Outline each blood parasite and name the species.
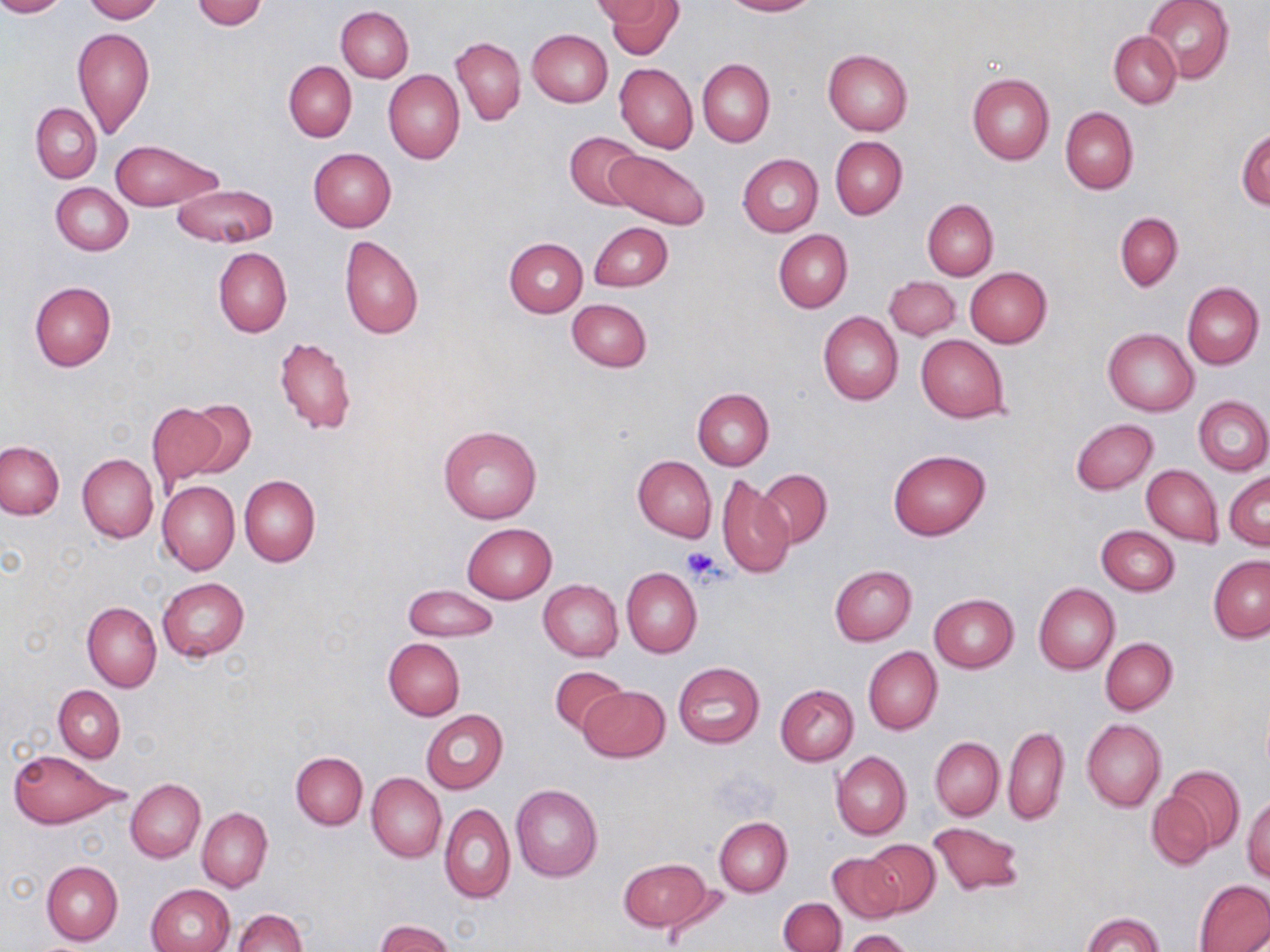
No blood parasites observed.

Summary:
  - Coordinate format: approximate bounding boxes as [x1, y1, x2, y2] in pixels
  - Uninfected red blood cell locations: [0, 0, 66, 17], [83, 0, 161, 22], [192, 0, 265, 29], [592, 0, 670, 24], [604, 0, 684, 59], [721, 0, 816, 16], [1141, 0, 1234, 85], [336, 6, 414, 81], [73, 27, 155, 138], [527, 29, 612, 107], [1109, 30, 1181, 108], [452, 37, 526, 125], [822, 49, 913, 135], [697, 58, 775, 146], [284, 60, 356, 142], [615, 63, 697, 153], [384, 70, 465, 164], [967, 74, 1054, 164], [32, 103, 102, 183], [1060, 107, 1139, 194], [1236, 127, 1269, 208], [565, 131, 644, 209], [830, 136, 908, 219], [110, 140, 217, 211], [309, 148, 395, 231], [605, 148, 709, 229], [737, 153, 822, 237], [51, 183, 132, 255], [171, 184, 278, 247], [923, 199, 998, 281], [1115, 212, 1183, 291], [590, 223, 672, 292], [774, 230, 853, 312], [338, 235, 424, 341], [503, 237, 588, 317], [213, 246, 291, 338], [965, 267, 1051, 347], [884, 277, 961, 340], [29, 281, 117, 370], [1182, 282, 1264, 370], [567, 299, 651, 372], [818, 310, 903, 405], [1103, 328, 1198, 416], [274, 336, 355, 436], [915, 336, 1010, 422], [693, 387, 774, 470], [1194, 395, 1269, 475], [184, 401, 256, 480], [147, 403, 227, 489], [1072, 418, 1157, 494], [438, 425, 542, 523], [0, 441, 64, 518], [887, 449, 991, 541], [77, 453, 158, 543], [632, 455, 716, 541], [1141, 465, 1223, 545], [758, 468, 832, 548], [1225, 472, 1270, 548], [717, 473, 796, 578], [239, 475, 320, 566], [157, 481, 239, 574], [463, 523, 556, 603], [1096, 526, 1179, 596], [1209, 555, 1270, 642], [829, 564, 917, 645], [622, 567, 702, 658], [157, 577, 250, 661], [539, 580, 623, 661], [1034, 583, 1119, 674], [404, 585, 498, 642], [929, 593, 1018, 672], [82, 601, 161, 691], [1100, 637, 1177, 715], [383, 638, 465, 720], [863, 646, 941, 735], [673, 662, 765, 748], [550, 665, 629, 736], [775, 684, 859, 765], [53, 685, 125, 761], [580, 686, 669, 763], [421, 710, 508, 794], [1081, 718, 1165, 812], [1003, 725, 1069, 824], [930, 736, 1004, 821], [8, 749, 124, 830], [291, 751, 367, 829], [831, 751, 911, 839], [1164, 764, 1246, 853], [367, 773, 446, 862], [125, 778, 205, 862], [511, 784, 604, 882], [1146, 788, 1216, 871], [1243, 793, 1270, 881], [440, 802, 514, 904], [197, 808, 272, 892], [714, 816, 792, 896], [927, 821, 1025, 898], [862, 839, 940, 916], [827, 851, 902, 923], [618, 857, 715, 932], [42, 859, 123, 945], [1194, 879, 1270, 952], [147, 884, 235, 952], [778, 898, 846, 952], [233, 909, 307, 952], [1082, 911, 1164, 952], [376, 920, 453, 952], [844, 929, 916, 952]
  - Platelet locations: [682, 547, 725, 583]
  - Slide-level diagnosis: negative for blood parasites
  - Modality: optical microscopy
  - Stain: May-Grünwald-Giemsa
  - Preparation: thin blood film
  - Image size: 1270×952 pixels
  - Magnification: 1000x
  - Field of view: single